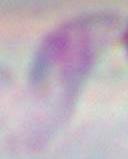

Captured at 1000x magnification. Photomicrograph. Toxoplasma gondii is seen.